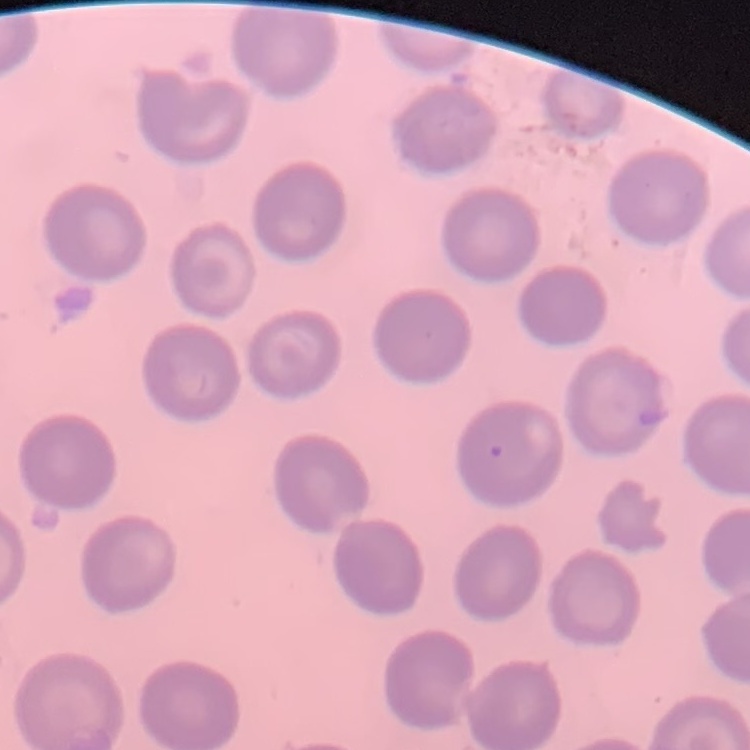
The red blood cells exhibit no rouleaux formation. Stained with either Field's or Giemsa. Thin blood film. Square crop of a larger photomicrograph.